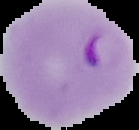
malaria status = parasitized
image size = 139×130 pixels
image type = cell region segmented out of the field of view; surrounding area masked to black
preparation = thin blood film